Identify the parasite.
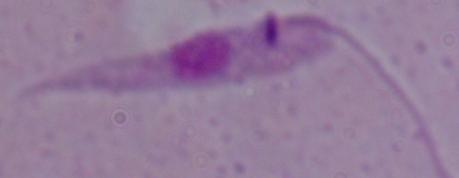
Leishmania.

Photomicrograph. 1000x magnification.